Report the malaria status of this cell.
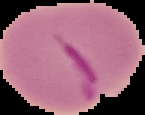

Parasitized.

image size = 145×115 pixels
preparation = thin blood smear
image type = segmented cell region on a black background